Assess this cell for malaria.
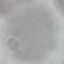

Uninfected.

Giemsa-stained preparation. Thin smear of blood. Automatically extracted cell patch, resized to 64 × 64 pixels. Acquired by smartphone through the microscope eyepiece.